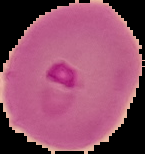

Summary:
  - Malaria status: parasitized
  - Image size: 145×154 pixels
  - Image type: segmented cell region with the area outside set to black
  - Preparation: thin blood smear